Report the malaria status of this cell.
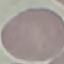

It is uninfected.

{
  "preparation": "thin smear",
  "capture": "smartphone camera at the microscope eyepiece",
  "image_type": "automatically extracted cell patch, resized to 64 × 64 pixels",
  "stain": "Giemsa"
}